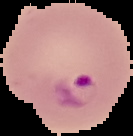

Result: malaria parasites detected. Image is 133×136 pixels. Segmented cell region on a black background. From a thin blood smear.